Classify this cell by malaria status.
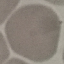

Uninfected.

Summary:
  - Preparation: thin blood smear
  - Capture: smartphone camera at the microscope eyepiece
  - Stain: Giemsa
  - Image type: cell patch, automatically extracted from a larger field of view and resized to 64 × 64 pixels